Point out each Plasmodium parasite.
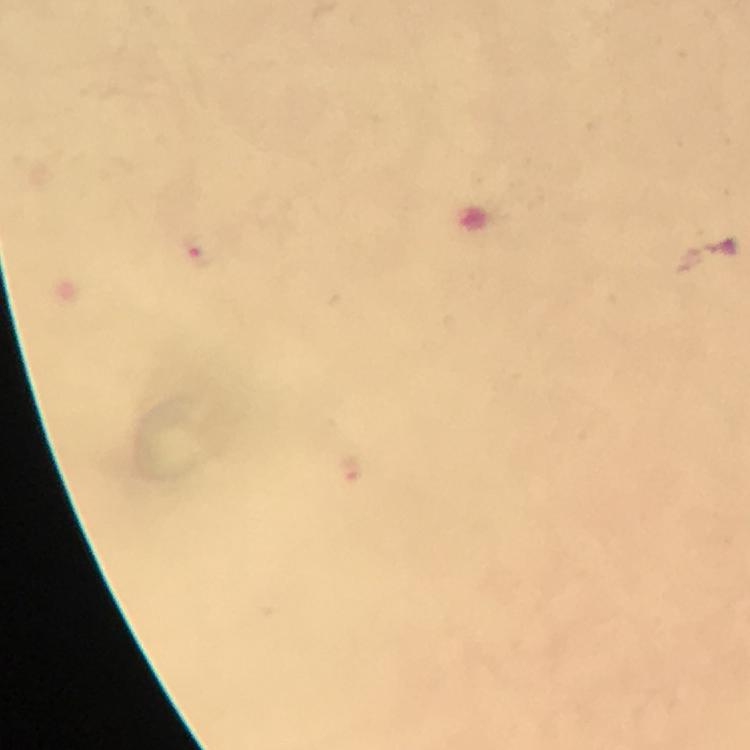

Approximate centers as [x, y] in pixels.
Plasmodium parasites: [197, 255].

Giemsa stain. A crop from one field of view. Thick blood film. At 100x magnification. Immersion oil applied. Image is 750×750 pixels. Smartphone photograph taken through a microscope. From a diagnostic examination for malaria.